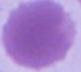

identification: erythrocyte
modality: photomicrograph
magnification: 1000x